Assess this cell for malaria.
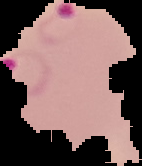

It is parasitized.

preparation = thin blood smear
image size = 142×166 pixels
image type = cell region segmented out of the field of view; surrounding area masked to black